Report the malaria status of this cell.
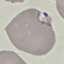

It is parasitized.

{
  "image_type": "cell patch, automatically extracted from a larger field of view and resized to 64 × 64 pixels",
  "stain": "Giemsa",
  "capture": "smartphone camera at the microscope eyepiece",
  "preparation": "thin blood film"
}